Classify this cell by malaria status.
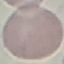

It is uninfected.

Summary:
  - Image type: cell patch, automatically extracted from a larger field of view and resized to 64 × 64 pixels
  - Stain: Giemsa
  - Preparation: thin blood film
  - Capture: smartphone through the microscope eyepiece